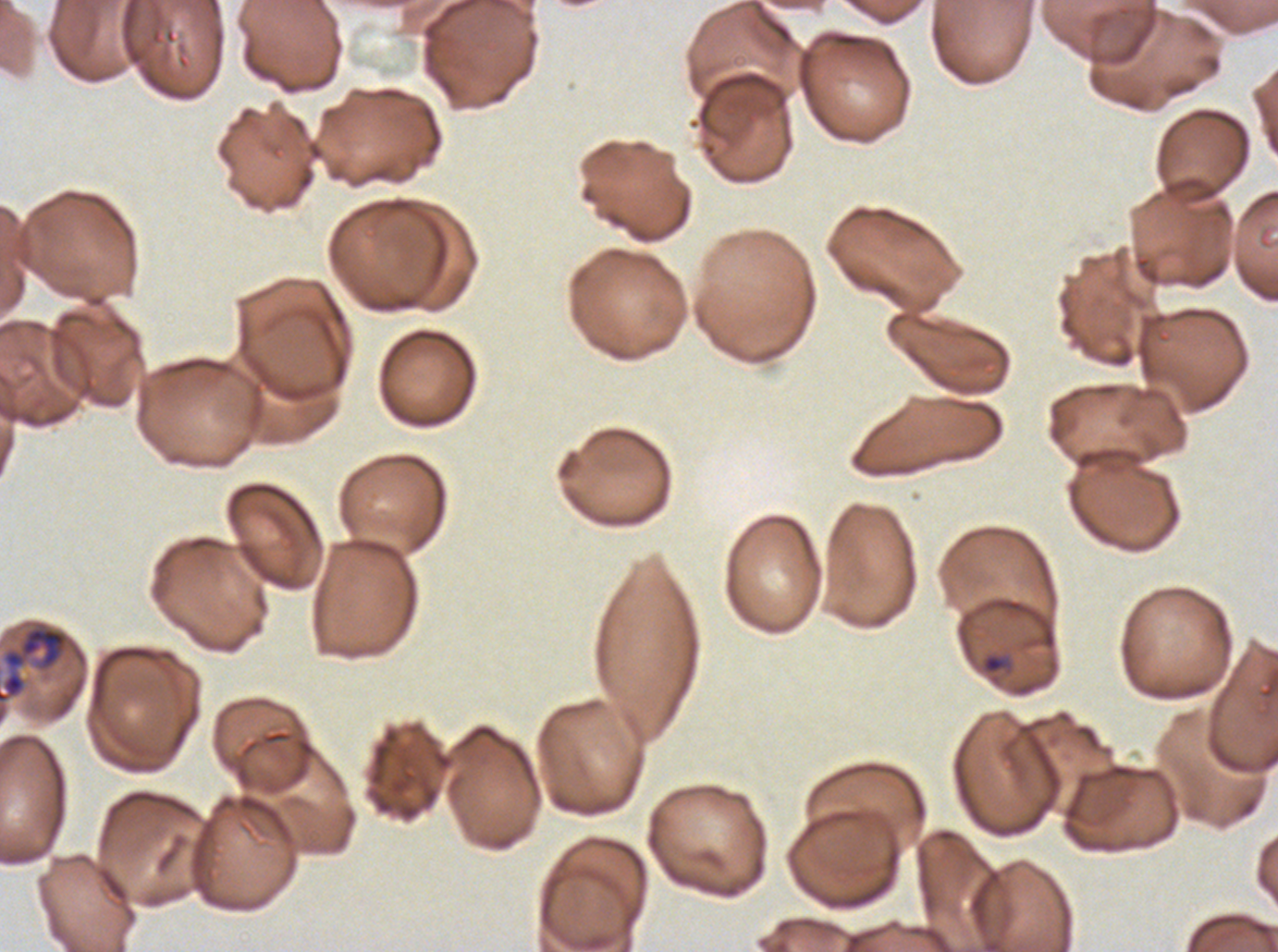

Approximate bounding boxes as {x1, y1, x2, y2} in pixels.
Summary:
  - Ring locations: {981, 653, 1008, 675}
  - Mid trophozoite locations: {0, 625, 69, 704}
  - Life-cycle stages observed: ring, mid trophozoite
  - Image size: 1278×952 pixels
  - Stain: Giemsa
  - Field of view: sub-image separated from a larger composite
  - Specimen: P. falciparum cultured ex vivo for 24 to 48 hours, from a patient in The Gambia
  - Preparation: thin blood film